Identify the cell.
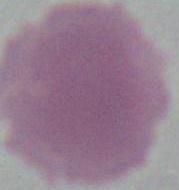

An erythrocyte.

Summary:
  - Magnification: 1000x
  - Modality: micrograph